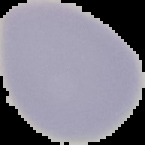
image_type: segmented cell region on a black background
result: no Plasmodium parasites detected
image_size: 145×145 pixels
preparation: thin blood film